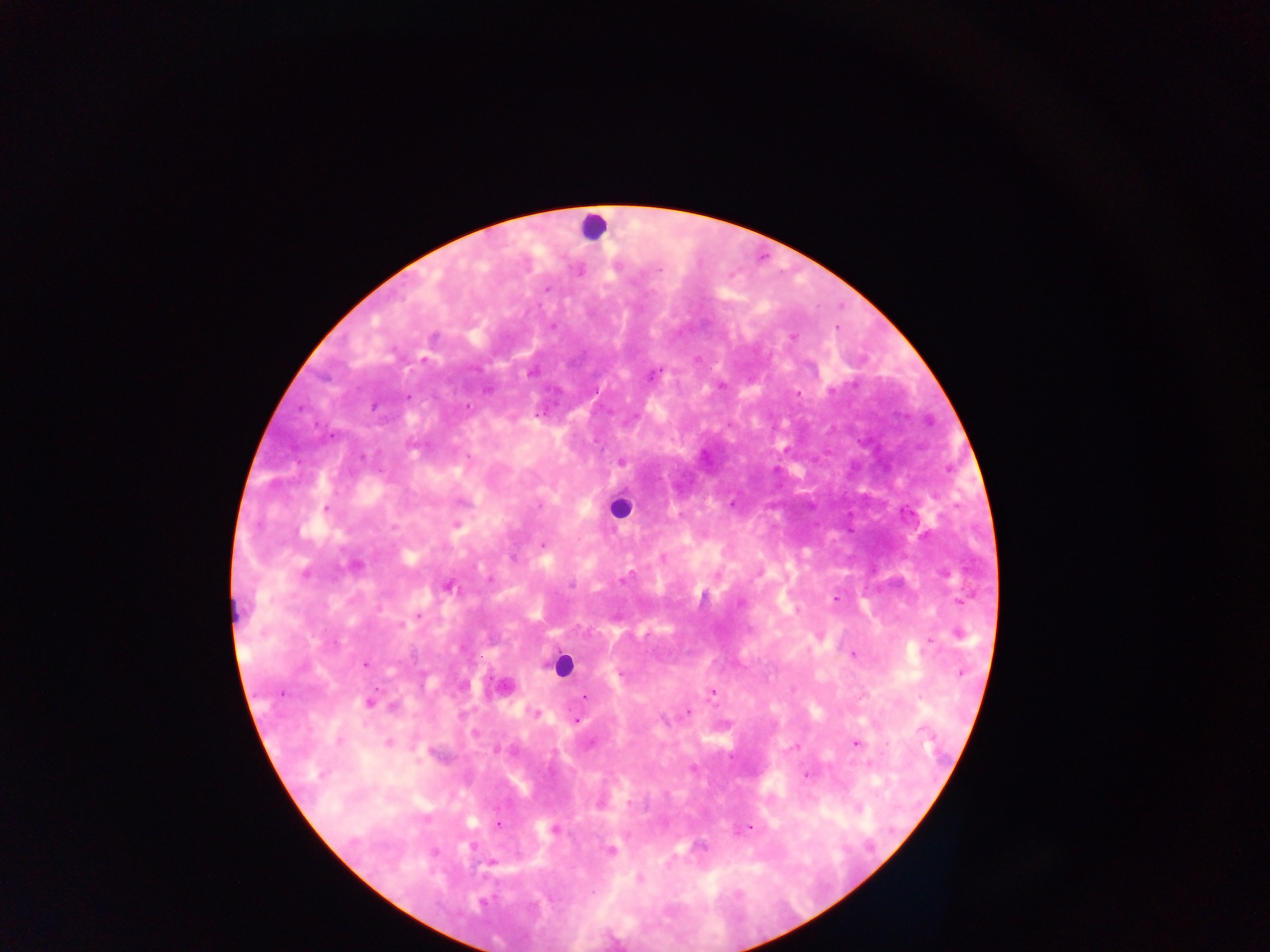

Approximate centers as (x, y) in pixels. Leukocyte locations: (593, 227), (619, 508), (562, 665). Plasmodium parasite locations: (579, 270), (791, 337), (651, 375), (797, 392), (465, 406), (621, 461), (732, 503), (326, 508), (456, 524), (542, 545), (663, 558), (354, 565), (945, 573), (448, 586), (835, 597), (417, 614), (957, 633), (820, 635), (853, 653), (366, 663), (503, 687), (712, 692), (585, 697), (369, 702), (685, 710), (536, 713), (576, 719), (388, 742), (854, 742), (600, 801), (497, 825), (750, 828), (554, 829), (609, 850), (490, 861), (639, 878). Thick blood film. Image is 1270×952 pixels. Collected in Ghana. Photographed through a microscope with a mobile-phone camera. Single field of view.